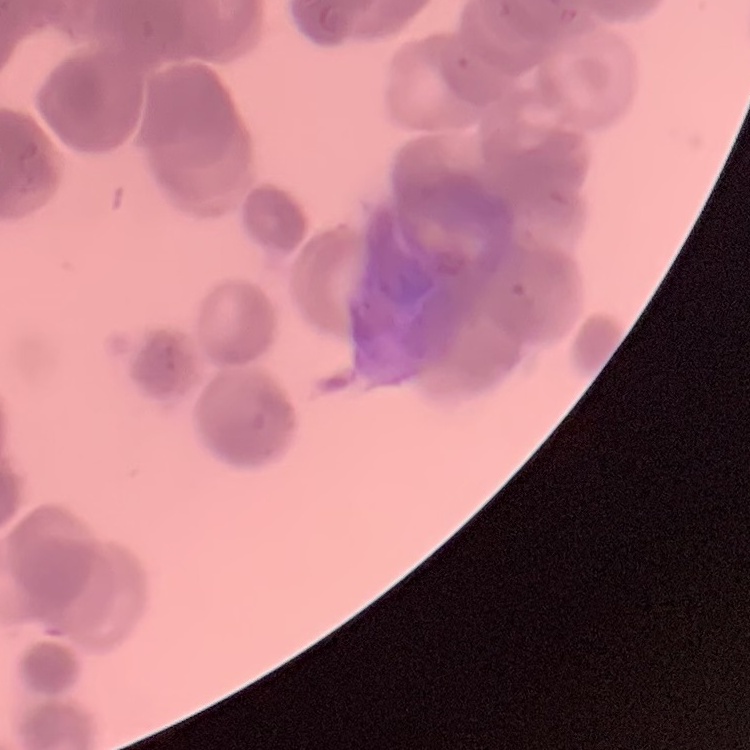
erythrocyte morphology = rouleaux formation
preparation = thin blood film
stain = Field's or Giemsa
image type = one tile cut from a larger photomicrograph